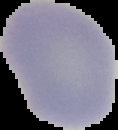
Summary:
  - Image size: 118×130 pixels
  - Image type: segmented cell region on a black background
  - Malaria status: uninfected
  - Preparation: thin blood film